Report the malaria status of this cell.
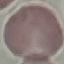

Uninfected.

Thin blood smear. Automatically extracted cell patch, resized to 64 × 64 pixels. Giemsa stain. Acquired by smartphone through the microscope eyepiece.